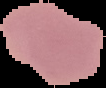 Image is 106×88 pixels. Malaria status: uninfected. Cell region segmented out of the field of view; the surrounding area is masked to black. From a thin blood smear.